State the blood parasite species.
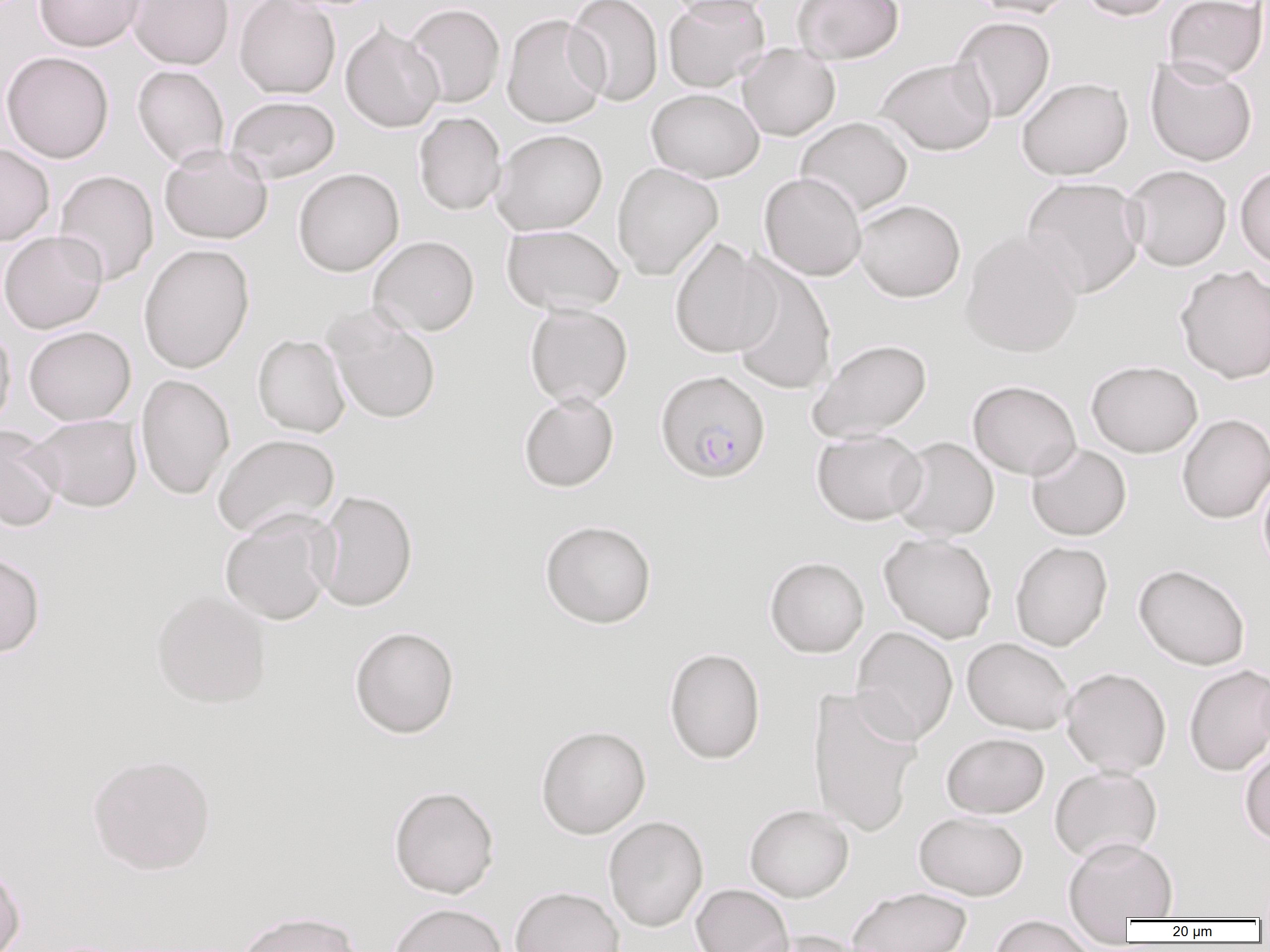

Plasmodium falciparum.

Summary:
  - Coordinate format: approximate bounding boxes as (x1,y1)-(x2,y2) corner pairs in pixels
  - Plasmodium falciparum-infected red blood cell locations: (654,369)-(771,483)
  - Uninfected red blood cell locations: (34,0)-(145,52), (127,0)-(234,69), (234,0)-(341,99), (564,0)-(663,106), (661,0)-(779,21), (663,0)-(769,92), (792,0)-(904,63), (969,0)-(1078,18), (1078,0)-(1176,21), (1164,0)-(1268,83), (404,3)-(505,108), (502,13)-(609,128), (951,15)-(1056,122), (340,22)-(444,133), (737,44)-(841,141), (1,51)-(114,163), (1145,56)-(1258,167), (876,57)-(996,155), (132,65)-(230,168), (1016,77)-(1133,180), (646,88)-(764,183), (226,95)-(340,184), (413,111)-(507,216), (795,117)-(913,217), (491,129)-(608,235), (0,144)-(54,246), (159,144)-(273,244), (612,162)-(724,280), (1235,164)-(1270,269), (1123,165)-(1232,271), (293,167)-(404,276), (53,169)-(159,286), (759,172)-(867,281), (1021,176)-(1146,298), (853,199)-(965,302), (501,224)-(624,315), (960,229)-(1084,358), (0,230)-(108,334), (368,235)-(480,336), (669,237)-(779,359), (138,243)-(255,374), (727,258)-(837,396), (1175,264)-(1270,384), (524,304)-(633,408), (325,308)-(441,425), (0,323)-(15,436), (23,326)-(136,425), (252,334)-(351,437), (808,338)-(931,442), (1086,359)-(1203,457), (135,373)-(235,500), (968,380)-(1082,479), (518,392)-(619,492), (1177,413)-(1270,524), (26,414)-(143,512), (0,425)-(63,531), (811,429)-(927,525), (212,434)-(340,539), (890,437)-(999,541), (1027,443)-(1132,541), (1257,466)-(1270,579), (313,490)-(418,612), (219,509)-(339,626), (540,519)-(657,628), (878,532)-(997,643), (1010,540)-(1113,651), (0,552)-(46,658), (765,556)-(869,658), (1133,563)-(1251,670), (151,589)-(272,708), (349,626)-(460,738), (851,626)-(959,745), (962,637)-(1075,735), (664,647)-(766,764), (1183,664)-(1270,776), (1060,666)-(1172,776), (806,685)-(924,838), (535,725)-(651,838), (941,732)-(1049,818), (1239,746)-(1270,846), (87,753)-(216,875), (1049,766)-(1163,864), (388,785)-(500,899), (745,804)-(854,902), (914,811)-(1028,901), (603,816)-(709,933), (1063,836)-(1179,923), (0,860)-(25,952), (690,884)-(794,952), (510,886)-(625,952), (847,887)-(972,952), (388,902)-(507,952), (236,910)-(363,952), (987,915)-(1097,952), (740,930)-(866,952)
  - Preparation: thin blood smear
  - Field of view: one of a larger specimen
  - Modality: light microscopy
  - Magnification: 1000x
  - Image size: 1270×952 pixels